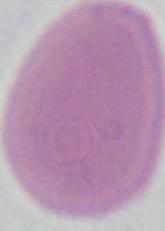

Summary:
  - Modality: micrograph
  - Identification: erythrocyte
  - Magnification: 1000x